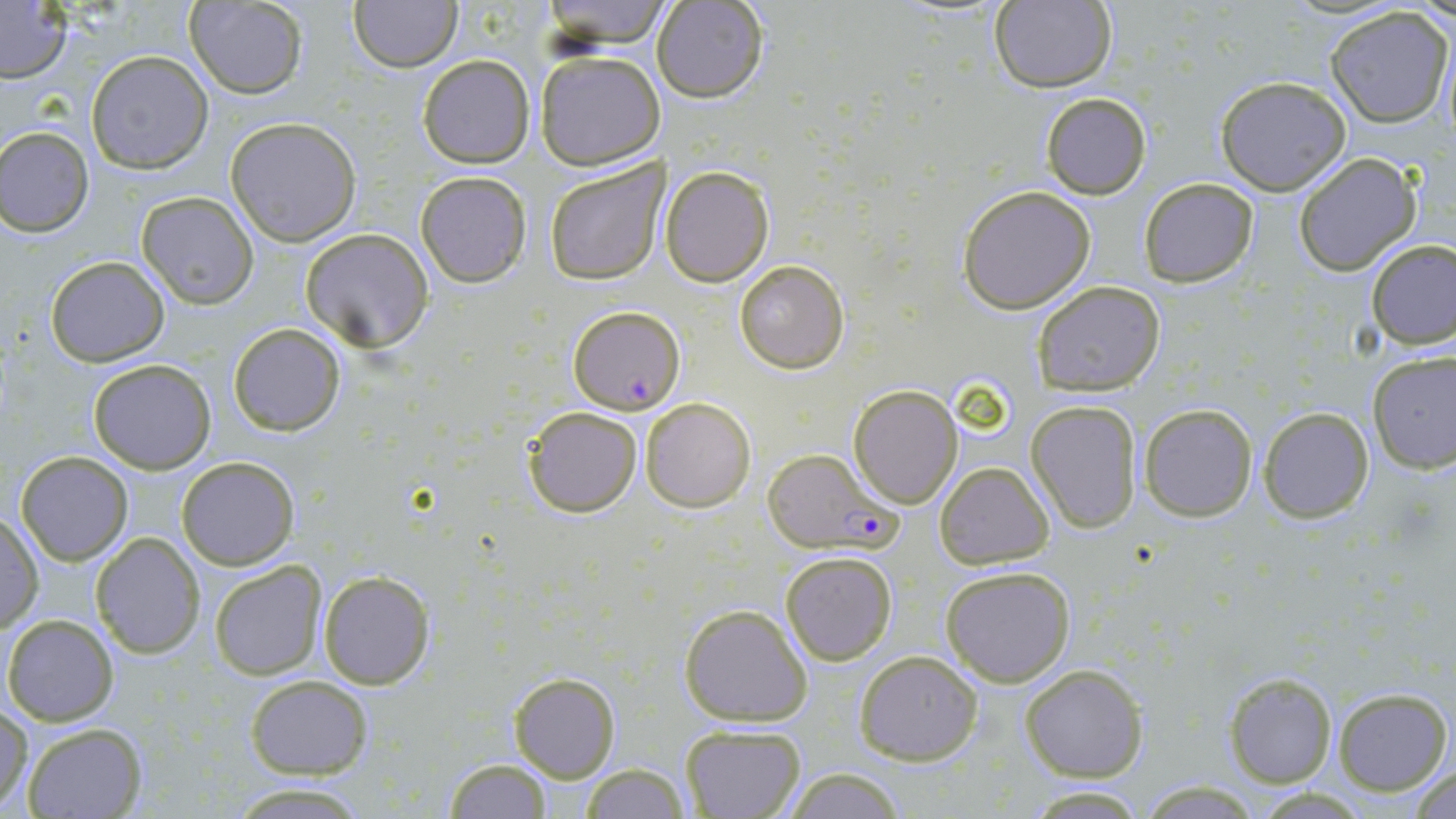

slide-level diagnosis = Plasmodium falciparum
stain = May-Grünwald-Giemsa
magnification = 1000x
Plasmodium falciparum-infected red blood cell locations = approximate bounding boxes as named x1/y1/x2/y2 corners in pixels: (x1=567, y1=306, x2=684, y2=414), (x1=761, y1=449, x2=893, y2=553)
field of view = single
image size = 1456×819 pixels
preparation = thin blood film
modality = light microscopy
uninfected red blood cell locations = approximate bounding boxes as named x1/y1/x2/y2 corners in pixels: (x1=183, y1=0, x2=309, y2=99), (x1=350, y1=0, x2=463, y2=72), (x1=536, y1=1, x2=673, y2=47), (x1=657, y1=1, x2=768, y2=103), (x1=988, y1=1, x2=1118, y2=92), (x1=0, y1=3, x2=72, y2=83), (x1=1322, y1=6, x2=1454, y2=128), (x1=534, y1=49, x2=665, y2=171), (x1=86, y1=50, x2=213, y2=174), (x1=417, y1=55, x2=534, y2=169), (x1=1214, y1=75, x2=1351, y2=195), (x1=1040, y1=93, x2=1150, y2=200), (x1=224, y1=116, x2=362, y2=247), (x1=1, y1=126, x2=95, y2=236), (x1=1293, y1=153, x2=1421, y2=275), (x1=544, y1=156, x2=669, y2=284), (x1=660, y1=165, x2=775, y2=286), (x1=414, y1=170, x2=533, y2=288), (x1=1138, y1=177, x2=1260, y2=288), (x1=955, y1=185, x2=1098, y2=314), (x1=136, y1=192, x2=259, y2=309), (x1=300, y1=228, x2=435, y2=352), (x1=1365, y1=239, x2=1455, y2=348), (x1=44, y1=256, x2=170, y2=367), (x1=734, y1=258, x2=850, y2=373), (x1=1033, y1=279, x2=1167, y2=395), (x1=227, y1=322, x2=346, y2=437), (x1=1368, y1=352, x2=1456, y2=475), (x1=87, y1=359, x2=216, y2=474), (x1=847, y1=383, x2=963, y2=509), (x1=641, y1=396, x2=758, y2=513), (x1=1026, y1=400, x2=1143, y2=534), (x1=1138, y1=403, x2=1259, y2=521), (x1=521, y1=405, x2=644, y2=518), (x1=1257, y1=406, x2=1375, y2=522), (x1=15, y1=451, x2=132, y2=566), (x1=176, y1=457, x2=300, y2=570), (x1=932, y1=461, x2=1055, y2=568), (x1=1, y1=512, x2=43, y2=634), (x1=91, y1=532, x2=206, y2=658), (x1=780, y1=550, x2=898, y2=665), (x1=209, y1=561, x2=326, y2=680), (x1=940, y1=564, x2=1077, y2=686), (x1=317, y1=569, x2=434, y2=690), (x1=679, y1=603, x2=812, y2=727), (x1=3, y1=614, x2=118, y2=725), (x1=853, y1=649, x2=984, y2=765), (x1=1020, y1=663, x2=1148, y2=782), (x1=1224, y1=672, x2=1337, y2=787), (x1=509, y1=673, x2=621, y2=782), (x1=246, y1=676, x2=373, y2=778), (x1=1331, y1=687, x2=1452, y2=796), (x1=1, y1=705, x2=33, y2=814), (x1=21, y1=722, x2=147, y2=818), (x1=679, y1=723, x2=805, y2=818), (x1=443, y1=759, x2=553, y2=817), (x1=578, y1=763, x2=689, y2=819), (x1=1409, y1=765, x2=1456, y2=818), (x1=780, y1=767, x2=909, y2=819), (x1=1135, y1=780, x2=1268, y2=816), (x1=228, y1=784, x2=369, y2=816), (x1=1021, y1=786, x2=1151, y2=817)